Locate and identify every blood parasite.
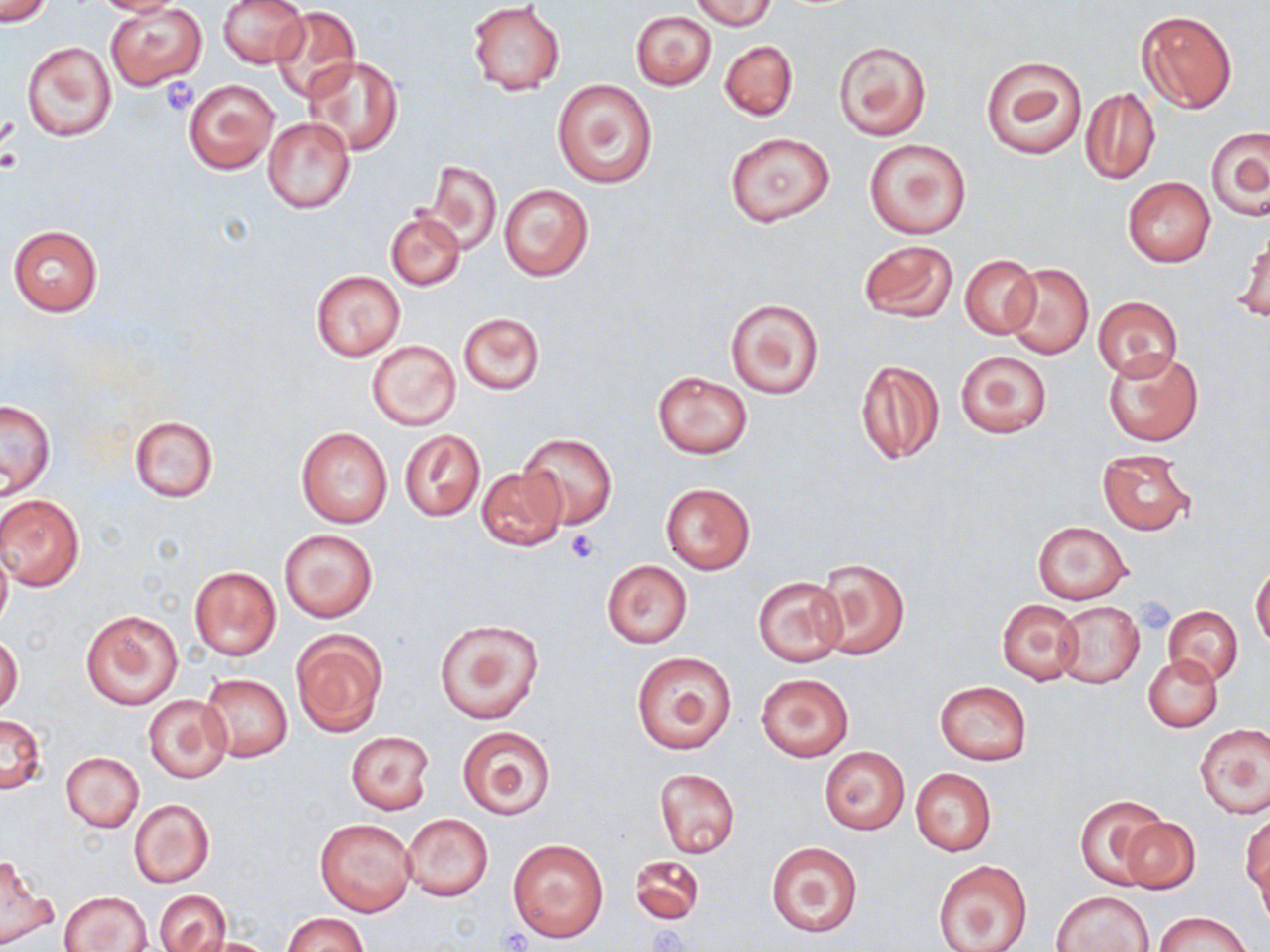
No blood parasites seen.

Approximate bounding boxes as (x1, y1, x2, y2) in pixels. Platelet locations: (160, 78, 198, 116), (0, 118, 20, 156), (1, 150, 20, 172), (565, 530, 603, 566), (1133, 596, 1175, 635), (648, 925, 690, 950), (502, 927, 532, 951). Uninfected red blood cell locations: (90, 0, 185, 16), (218, 0, 309, 67), (691, 0, 776, 30), (1, 1, 54, 26), (466, 4, 565, 96), (106, 5, 206, 89), (270, 7, 362, 103), (630, 9, 717, 90), (1137, 10, 1237, 114), (832, 39, 932, 142), (721, 40, 798, 120), (22, 41, 116, 142), (981, 55, 1087, 160), (305, 56, 403, 155), (184, 79, 277, 173), (551, 79, 658, 189), (1080, 86, 1160, 185), (262, 115, 356, 214), (1206, 125, 1269, 221), (725, 132, 835, 226), (863, 138, 972, 239), (425, 160, 501, 253), (398, 167, 490, 286), (1123, 177, 1216, 268), (498, 183, 594, 282), (387, 210, 465, 290), (8, 224, 104, 317), (1235, 227, 1269, 324), (858, 241, 958, 325), (959, 254, 1041, 339), (1004, 263, 1093, 360), (311, 270, 406, 361), (1092, 295, 1181, 378), (725, 297, 824, 399), (458, 312, 545, 394), (368, 339, 460, 431), (1102, 349, 1203, 446), (956, 350, 1051, 438), (855, 358, 945, 465), (653, 371, 752, 458), (0, 401, 55, 497), (130, 416, 218, 502), (296, 427, 393, 529), (401, 430, 486, 521), (518, 432, 616, 530), (1096, 448, 1196, 536), (477, 465, 566, 550), (661, 482, 755, 573), (0, 494, 85, 591), (1033, 521, 1132, 604), (279, 527, 378, 623), (0, 545, 12, 631), (813, 556, 911, 660), (601, 560, 692, 648), (1251, 565, 1270, 648), (189, 566, 281, 661), (753, 576, 845, 667), (996, 599, 1082, 684), (1054, 601, 1143, 689), (1164, 605, 1243, 685), (81, 609, 183, 709), (433, 616, 544, 724), (291, 631, 387, 735), (0, 636, 23, 714), (631, 651, 736, 754), (1144, 656, 1221, 732), (755, 672, 854, 762), (200, 673, 292, 762), (934, 682, 1032, 765), (143, 693, 235, 785), (1, 715, 46, 794), (1196, 723, 1269, 818), (456, 724, 557, 819), (346, 730, 436, 814), (819, 748, 909, 834), (61, 752, 144, 832), (654, 767, 739, 859), (910, 768, 996, 857), (1076, 795, 1167, 888), (130, 799, 215, 888), (402, 814, 493, 900), (1120, 815, 1200, 894), (1242, 815, 1269, 904), (315, 818, 417, 918), (509, 839, 608, 941), (767, 842, 863, 937), (630, 853, 705, 925), (0, 855, 56, 948), (933, 859, 1032, 952), (1054, 890, 1155, 952), (60, 891, 152, 952), (155, 891, 230, 952), (1156, 912, 1251, 952), (282, 913, 370, 952), (186, 936, 278, 952). Slide-level diagnosis: no evidence of blood parasites. 1000x magnification. Image is 1270×952 pixels. Optical microscopy. Thin blood smear. May-Grünwald-Giemsa stain. One field of a larger specimen.